State which cell type is depicted.
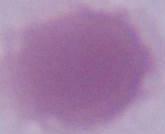

An erythrocyte.

modality = photomicrograph
magnification = 1000x